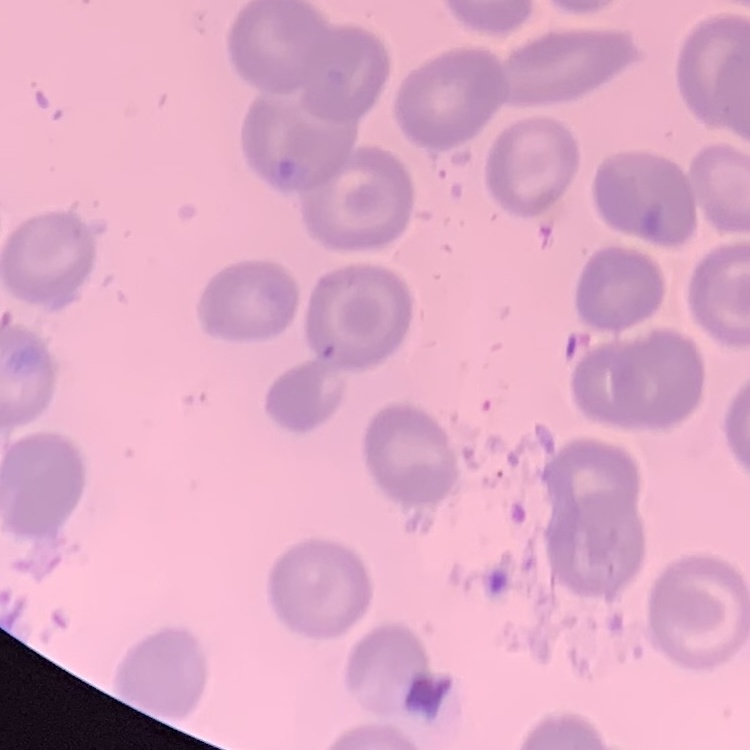
The red blood cells show no rouleaux formation. One tile cut from a larger photomicrograph. Field's or Giemsa stain. Thin peripheral smear.